Locate every blood parasite and identify its species.
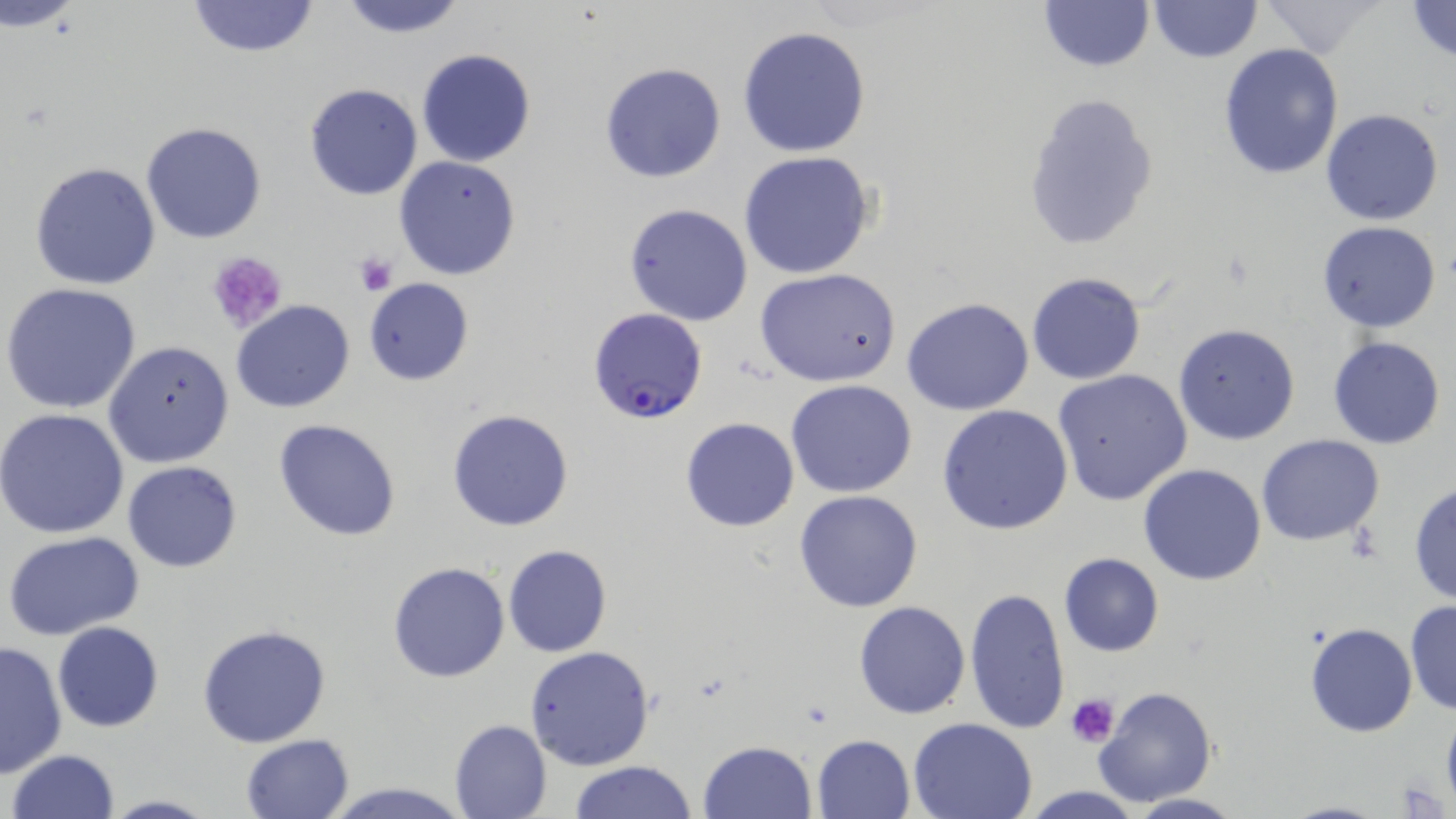
Approximate bounding boxes as named x1/y1/x2/y2 corners in pixels.
Plasmodium falciparum-infected red blood cells: (x1=589, y1=307, x2=709, y2=426).
No Plasmodium ovale, Plasmodium malariae, Plasmodium vivax, Babesia divergens, or Trypanosoma brucei observed.

slide-level diagnosis = Plasmodium falciparum
uninfected red blood cell locations = approximate bounding boxes as named x1/y1/x2/y2 corners in pixels: (x1=334, y1=0, x2=472, y2=38), (x1=1038, y1=0, x2=1156, y2=72), (x1=1403, y1=0, x2=1456, y2=65), (x1=184, y1=1, x2=320, y2=57), (x1=1148, y1=1, x2=1263, y2=63), (x1=4, y1=2, x2=89, y2=33), (x1=1260, y1=2, x2=1387, y2=58), (x1=738, y1=25, x2=872, y2=159), (x1=1217, y1=42, x2=1344, y2=180), (x1=416, y1=48, x2=537, y2=168), (x1=600, y1=62, x2=726, y2=184), (x1=303, y1=83, x2=423, y2=201), (x1=1021, y1=90, x2=1160, y2=252), (x1=1320, y1=108, x2=1445, y2=227), (x1=141, y1=121, x2=268, y2=244), (x1=736, y1=151, x2=877, y2=279), (x1=394, y1=155, x2=523, y2=281), (x1=29, y1=161, x2=161, y2=290), (x1=623, y1=203, x2=754, y2=326), (x1=1316, y1=221, x2=1442, y2=333), (x1=755, y1=269, x2=902, y2=386), (x1=1026, y1=272, x2=1146, y2=386), (x1=362, y1=278, x2=475, y2=386), (x1=2, y1=282, x2=144, y2=415), (x1=901, y1=297, x2=1034, y2=416), (x1=231, y1=299, x2=355, y2=413), (x1=1172, y1=323, x2=1299, y2=446), (x1=1327, y1=335, x2=1445, y2=449), (x1=103, y1=340, x2=234, y2=466), (x1=1052, y1=369, x2=1193, y2=507), (x1=787, y1=380, x2=916, y2=498), (x1=938, y1=404, x2=1074, y2=535), (x1=447, y1=408, x2=575, y2=532), (x1=0, y1=409, x2=130, y2=539), (x1=680, y1=416, x2=799, y2=532), (x1=273, y1=418, x2=402, y2=541), (x1=1257, y1=434, x2=1385, y2=545), (x1=121, y1=460, x2=244, y2=573), (x1=1138, y1=462, x2=1268, y2=585), (x1=1410, y1=481, x2=1456, y2=606), (x1=794, y1=490, x2=923, y2=612), (x1=3, y1=529, x2=145, y2=639), (x1=503, y1=544, x2=613, y2=657), (x1=1058, y1=553, x2=1165, y2=657), (x1=387, y1=562, x2=510, y2=683), (x1=964, y1=586, x2=1069, y2=733), (x1=1404, y1=598, x2=1456, y2=715), (x1=853, y1=601, x2=971, y2=719), (x1=52, y1=622, x2=163, y2=733), (x1=1306, y1=623, x2=1417, y2=736), (x1=195, y1=624, x2=332, y2=748), (x1=1, y1=640, x2=66, y2=779), (x1=524, y1=645, x2=657, y2=771), (x1=1095, y1=685, x2=1214, y2=807), (x1=5, y1=695, x2=92, y2=817), (x1=1441, y1=713, x2=1456, y2=807), (x1=908, y1=716, x2=1038, y2=819), (x1=448, y1=719, x2=551, y2=819), (x1=241, y1=734, x2=356, y2=819), (x1=810, y1=734, x2=915, y2=819), (x1=699, y1=740, x2=817, y2=818), (x1=8, y1=749, x2=121, y2=818), (x1=568, y1=760, x2=696, y2=818), (x1=319, y1=778, x2=469, y2=818), (x1=1013, y1=785, x2=1151, y2=818), (x1=1122, y1=792, x2=1245, y2=818), (x1=99, y1=794, x2=218, y2=818), (x1=1278, y1=799, x2=1394, y2=819)
platelet locations = approximate bounding boxes as named x1/y1/x2/y2 corners in pixels: (x1=204, y1=251, x2=289, y2=335), (x1=353, y1=252, x2=398, y2=297), (x1=1066, y1=692, x2=1117, y2=746), (x1=1394, y1=777, x2=1449, y2=817)
field of view = one of a larger specimen
image size = 1456×819 pixels
magnification = 1000x
modality = optical microscopy
stain = May-Grünwald-Giemsa
preparation = thin blood film